Describe the morphology of the red blood cells.
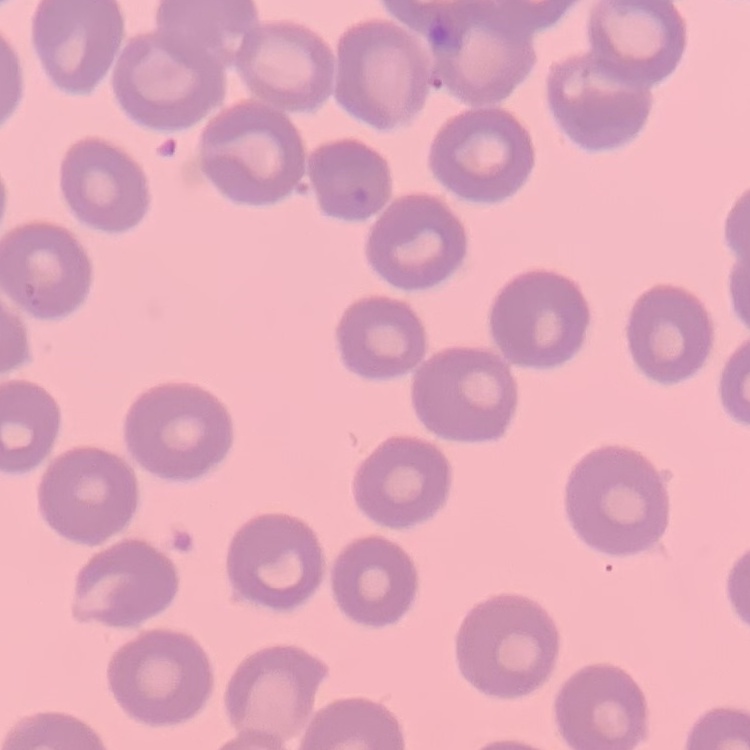

No rouleaux formation.

Summary:
  - Image type: one tile cut from a larger photomicrograph
  - Preparation: thin blood smear
  - Stain: Field's or Giemsa